Assess this cell for malaria.
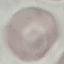
Uninfected.

Cell patch, automatically extracted from a larger field of view and resized to 64 × 64 pixels. Photographed with a smartphone camera at the microscope eyepiece. Thin blood smear. Giemsa-stained preparation.